Point out each malaria parasite.
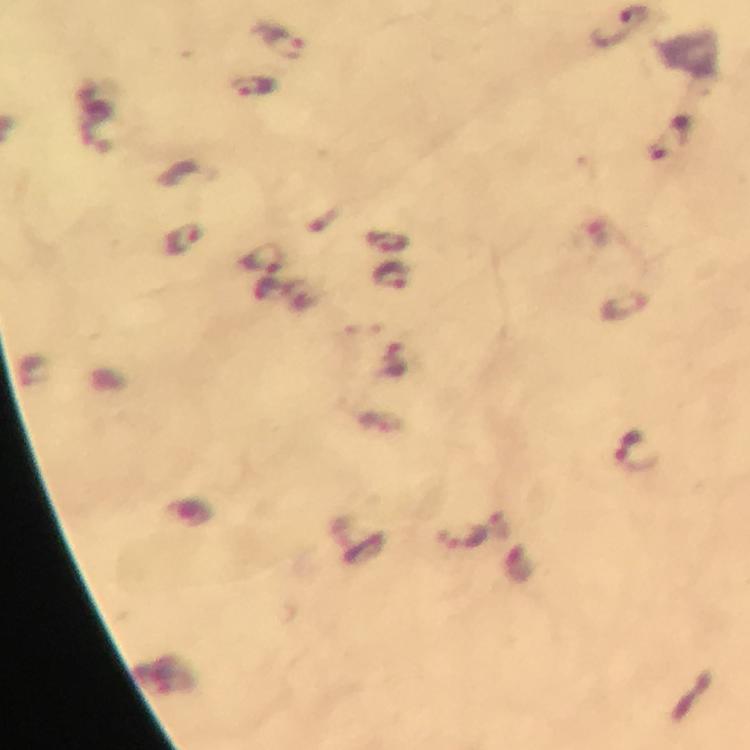

Approximate centers as {x, y} in pixels.
Malaria parasites: {283, 43}, {253, 86}, {183, 237}, {263, 257}, {390, 274}, {625, 306}, {632, 449}, {460, 536}.

{
  "context": "from a diagnostic examination for malaria",
  "immersion_oil": "used",
  "cropped_from": "a single field of view",
  "magnification": "100x",
  "image_size": "750×750 pixels",
  "capture": "smartphone camera through the microscope",
  "preparation": "thick blood film",
  "stain": "Giemsa"
}